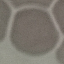
result = no malaria parasites seen
preparation = thin blood smear
capture = smartphone through the microscope eyepiece
stain = Giemsa
image type = cell patch, automatically extracted from a larger field of view and resized to 64 × 64 pixels